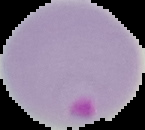
image size = 145×130 pixels
result = Plasmodium parasites detected
preparation = thin blood smear
image type = cell region segmented out of the field of view; surrounding area masked to black